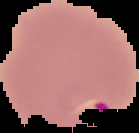

image size = 139×133 pixels
malaria status = parasitized
preparation = thin blood film
image type = segmented cell region with the area outside set to black